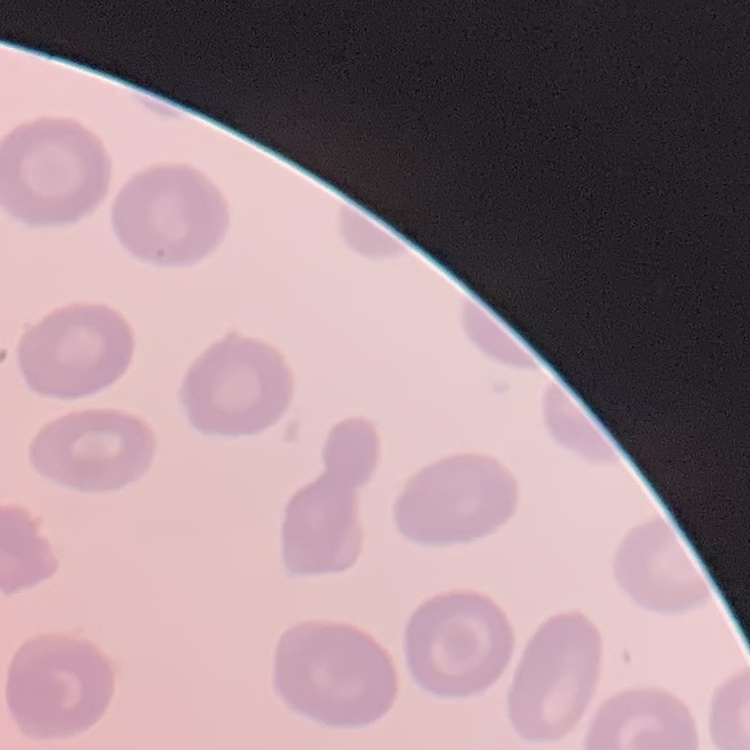
red blood cell morphology = no rouleaux formation
image type = one tile cut from a larger photomicrograph
preparation = thin peripheral smear
stain = Field's or Giemsa